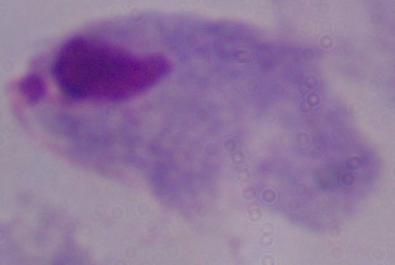
Summary:
  - Magnification: 1000x
  - Modality: micrograph
  - Identification: trichomonad